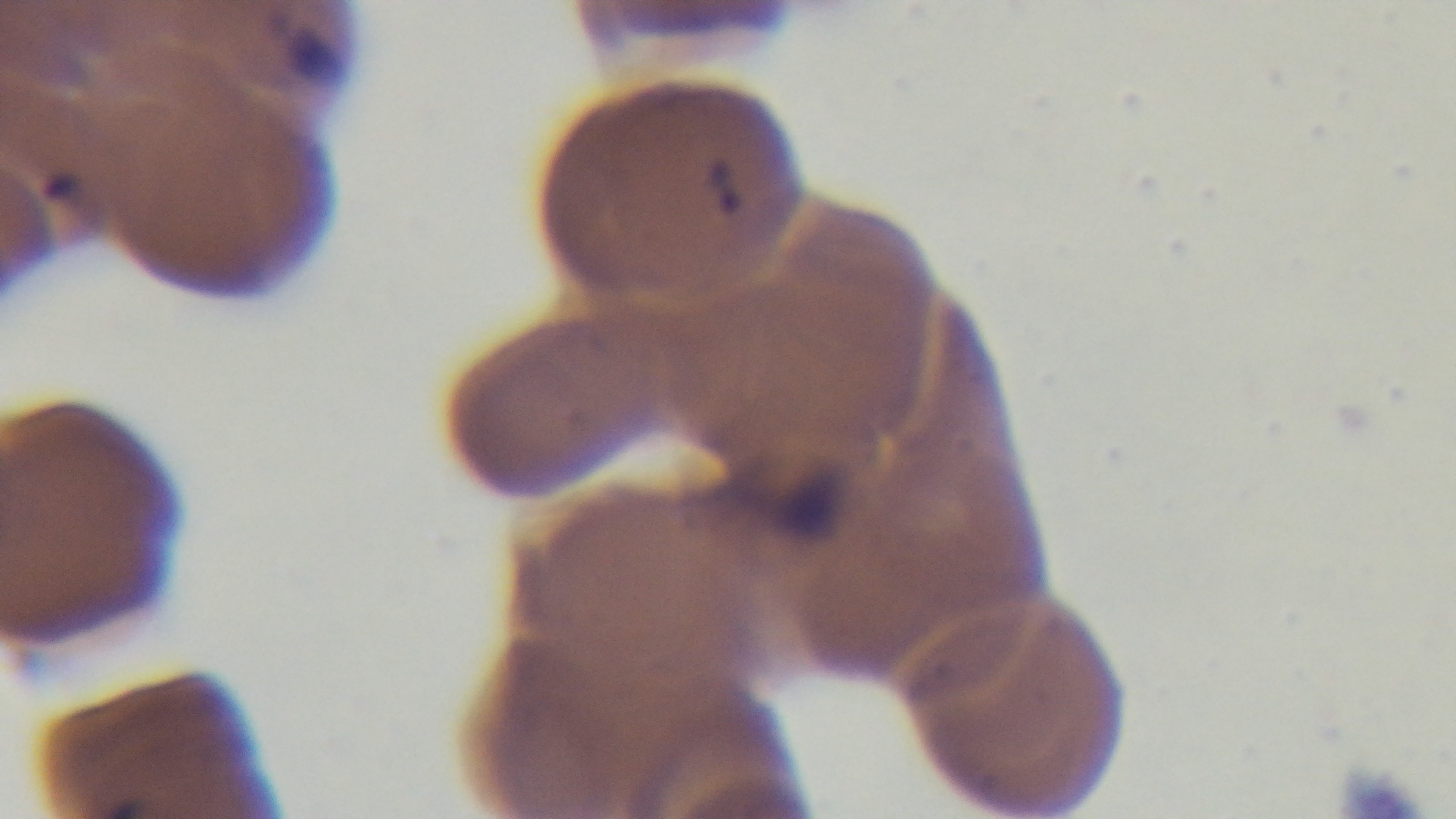

Mounted 4K digital camera. Single field of view. 100x oil-immersion objective. Malaria status: infected. Giemsa-stained. Light microscopy. Preparation: thin smear.